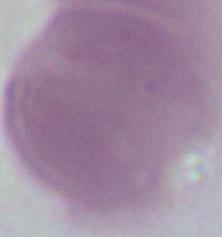 1000x magnification. Photomicrograph. An erythrocyte is shown.